Give the position of every malaria parasite.
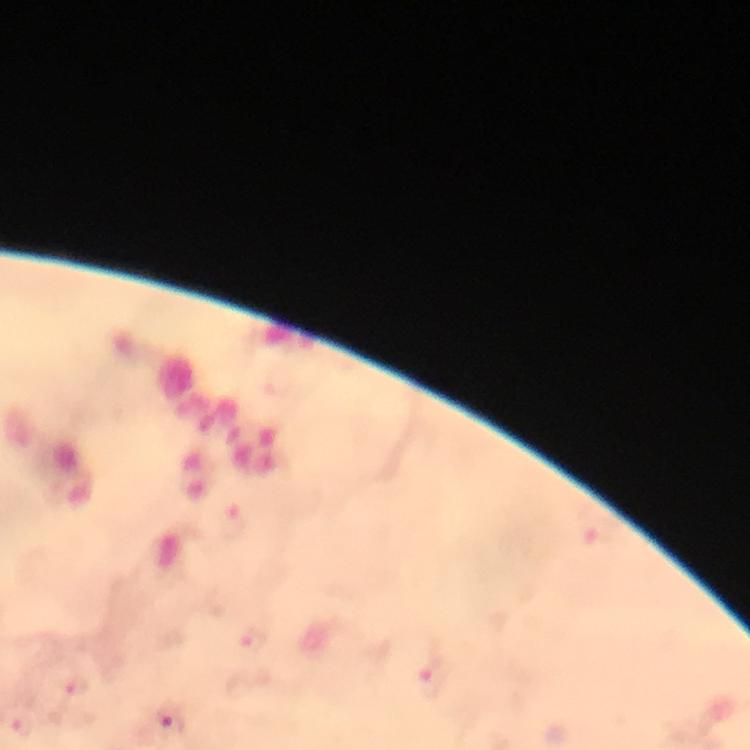
Approximate object centers, in pixels from the top-left corner.
Malaria parasites: (x=253, y=641), (x=432, y=679), (x=76, y=687), (x=171, y=719), (x=21, y=727).

Giemsa stain. Immersion oil was used. Image is 750×750 pixels. Thick smear. From a diagnostic examination for malaria. Smartphone photograph taken through a microscope. A crop from one field of view. At 100x magnification.